Locate every blood parasite and identify its species.
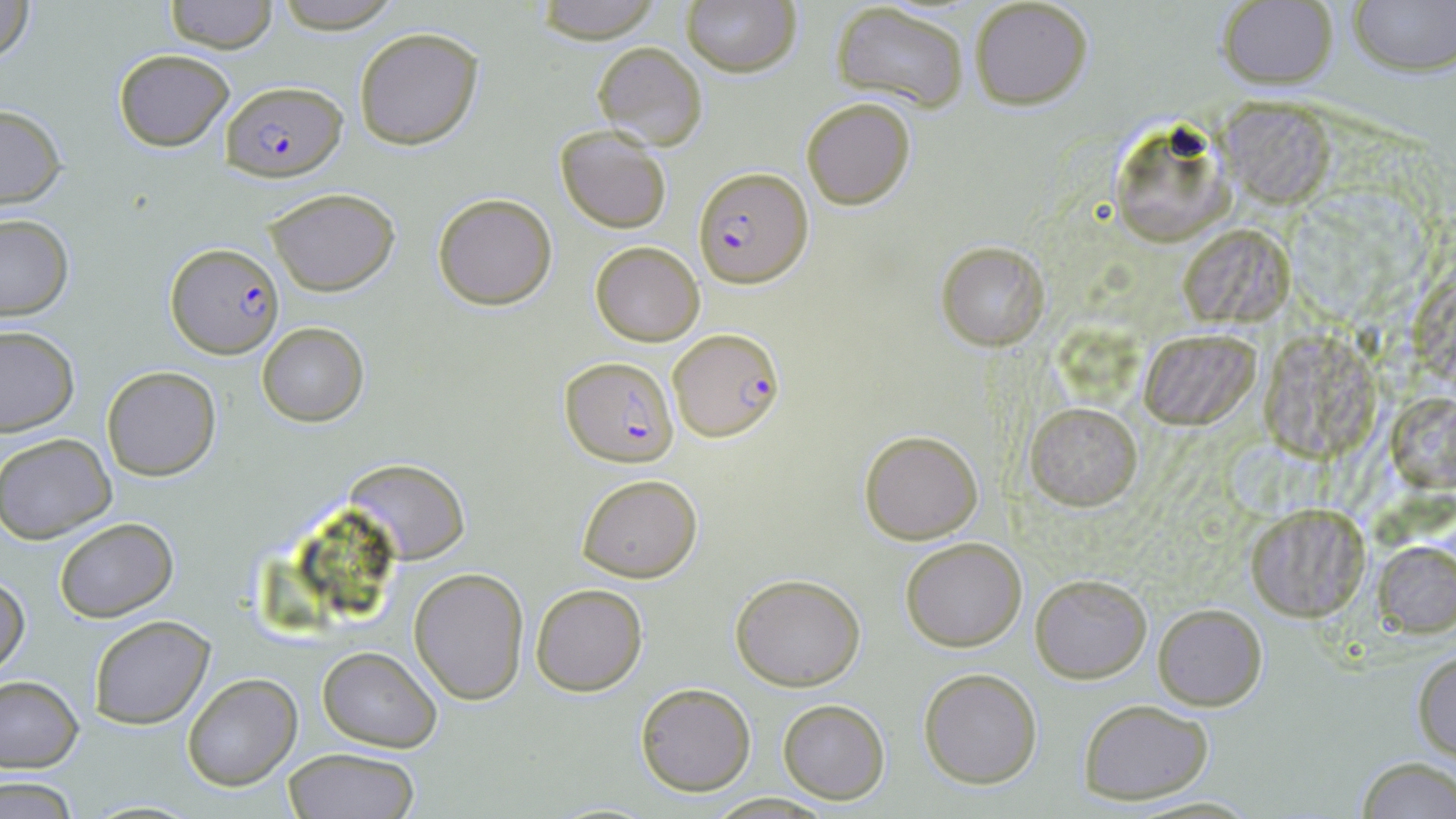
Approximate bounding boxes as (x1, y1, x2, y2) in pixels.
Plasmodium falciparum-infected red blood cells: (219, 78, 347, 177), (692, 165, 812, 289), (166, 242, 285, 359), (670, 328, 783, 441), (560, 356, 678, 467).
No Plasmodium ovale, Plasmodium malariae, Plasmodium vivax, Babesia divergens, or Trypanosoma brucei observed.

Uninfected red blood cell locations: (0, 0, 37, 63), (268, 0, 403, 34), (532, 0, 664, 43), (969, 0, 1094, 111), (1348, 0, 1455, 75), (166, 1, 276, 53), (681, 1, 802, 79), (1216, 1, 1337, 92), (830, 3, 970, 110), (354, 26, 484, 149), (590, 41, 708, 150), (112, 48, 235, 151), (801, 97, 917, 210), (1222, 100, 1335, 206), (0, 104, 67, 209), (1107, 113, 1240, 248), (555, 128, 672, 234), (263, 186, 402, 296), (433, 193, 558, 311), (0, 215, 74, 321), (1186, 226, 1295, 320), (936, 241, 1049, 351), (590, 242, 703, 346), (1402, 271, 1455, 385), (256, 322, 368, 426), (0, 326, 78, 437), (1137, 328, 1257, 428), (1263, 330, 1381, 462), (100, 365, 222, 481), (1392, 393, 1453, 491), (1025, 402, 1142, 509), (858, 428, 984, 545), (1, 432, 117, 542), (346, 458, 469, 563), (576, 472, 704, 584), (1246, 503, 1369, 622), (54, 517, 178, 622), (899, 536, 1027, 652), (1373, 540, 1456, 638), (408, 567, 528, 705), (731, 571, 867, 692), (0, 572, 29, 675), (1029, 573, 1152, 681), (530, 582, 649, 697), (1153, 604, 1267, 711), (88, 615, 215, 729), (317, 647, 442, 752), (1412, 651, 1456, 761), (918, 667, 1042, 789), (182, 674, 302, 791), (0, 677, 83, 772), (634, 681, 757, 795), (776, 698, 890, 803), (1080, 698, 1215, 803), (283, 747, 420, 819), (1354, 755, 1456, 819), (1, 778, 79, 817), (702, 792, 841, 818). Slide-level diagnosis: Plasmodium falciparum. 1000x magnification. Optical microscopy. May-Grünwald-Giemsa-stained preparation. Image is 1456×819 pixels. Thin blood film. Single field of view.